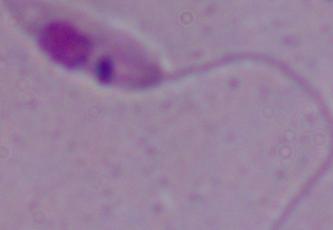
magnification = 1000x
identification = Leishmania
modality = photomicrograph